Comment on the morphology of the red blood cells.
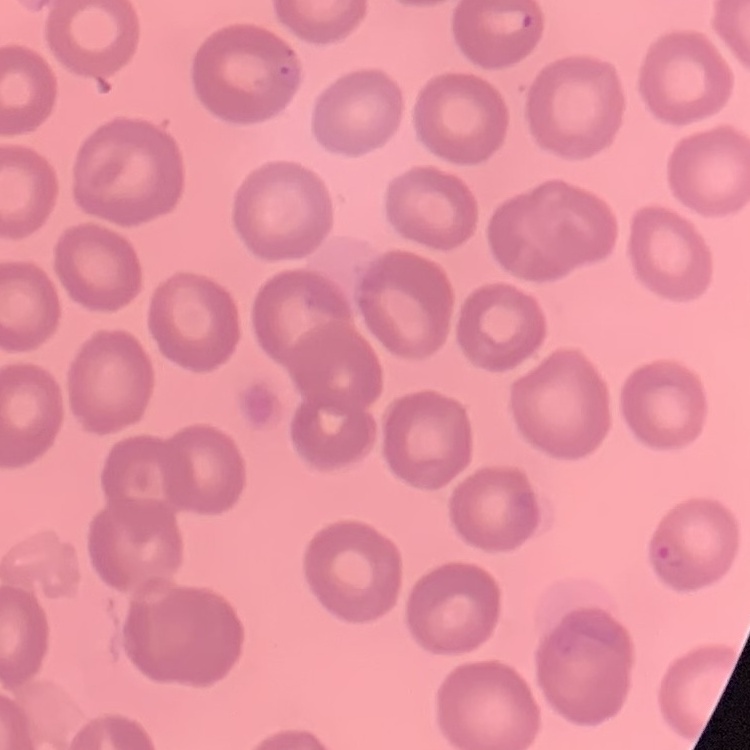
No rouleaux formation.

image type = one tile cut from a larger photomicrograph
preparation = thin peripheral smear
stain = Field's or Giemsa